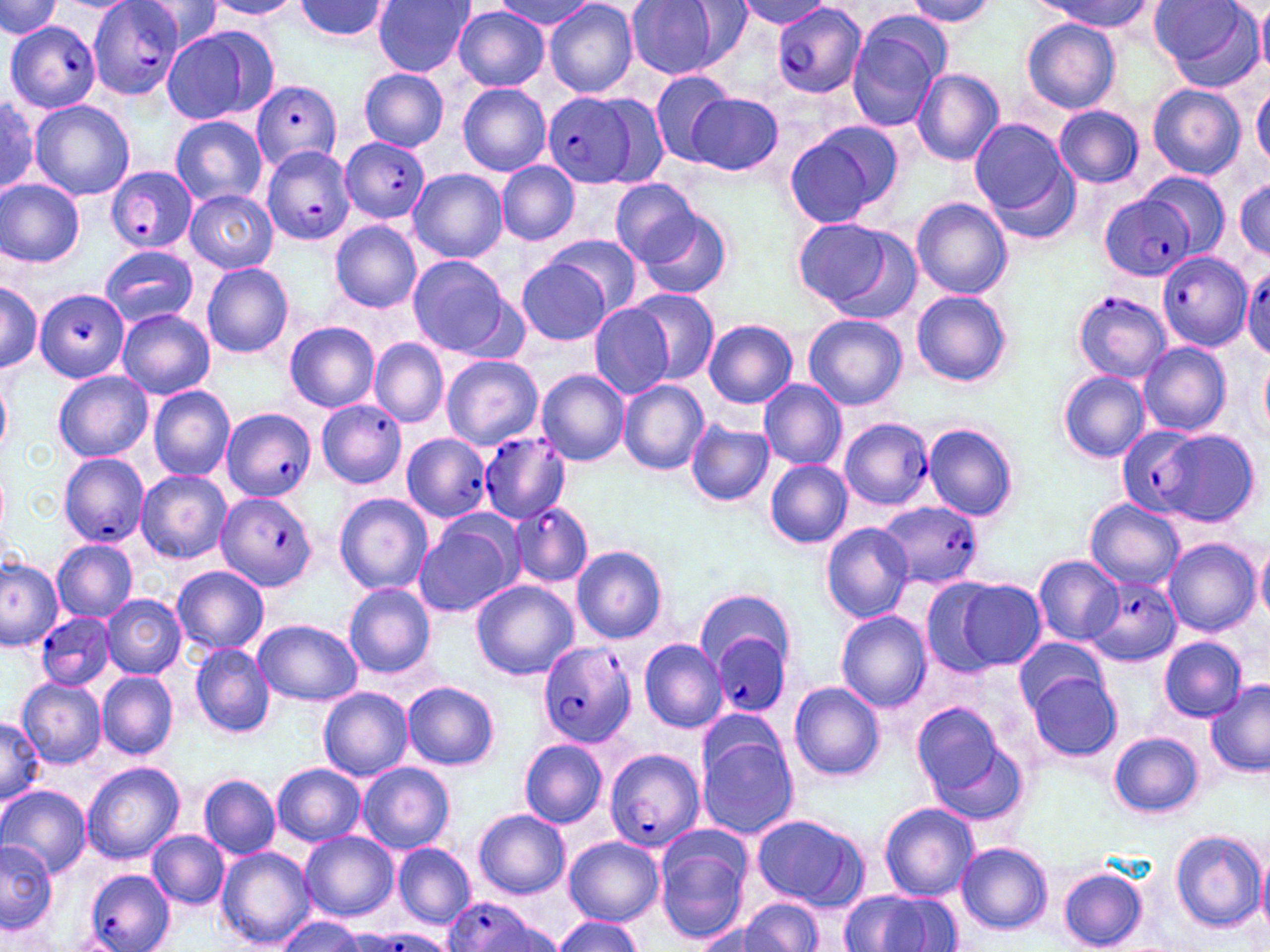

{
  "slide_level_diagnosis": "Plasmodium falciparum",
  "image_size": "1270×952 pixels",
  "uninfected_red_blood_cell_locations": "approximate bounding boxes as (x1,y1)-(x2,y2) corner pairs in pixels: (0,0)-(59,38), (287,0)-(396,44), (497,0)-(596,31), (627,0)-(724,79), (732,0)-(833,30), (1039,0)-(1151,32), (1153,0)-(1265,91), (134,1)-(227,53), (201,1)-(302,20), (371,1)-(475,76), (544,1)-(638,98), (907,1)-(994,28), (681,2)-(753,69), (1255,3)-(1270,76), (452,6)-(549,90), (847,16)-(948,131), (1022,18)-(1120,113), (159,25)-(277,127), (864,41)-(981,156), (913,68)-(1004,167), (360,69)-(449,149), (647,69)-(737,167), (458,82)-(551,175), (1148,83)-(1245,179), (1251,83)-(1270,170), (686,92)-(783,176), (0,97)-(45,197), (29,100)-(134,203), (1055,105)-(1143,188), (171,115)-(268,207), (969,119)-(1078,228), (784,122)-(900,228), (498,161)-(579,245), (408,168)-(507,263), (1140,170)-(1229,260), (1234,177)-(1269,259), (0,179)-(85,267), (610,180)-(702,266), (185,190)-(278,273), (913,197)-(1011,298), (633,206)-(734,301), (789,215)-(917,320), (330,220)-(421,312), (544,234)-(642,319), (100,246)-(198,327), (406,254)-(517,358), (515,259)-(613,346), (201,263)-(293,358), (0,282)-(42,371), (626,287)-(720,385), (912,290)-(1012,386), (589,304)-(673,397), (117,310)-(214,399), (803,314)-(908,410), (703,319)-(798,407), (285,322)-(379,412), (370,339)-(447,427), (1137,342)-(1230,437), (1258,353)-(1270,439), (441,355)-(543,449), (536,369)-(629,466), (1057,370)-(1151,464), (54,371)-(152,462), (0,376)-(11,456), (618,379)-(709,475), (758,379)-(846,470), (149,385)-(235,481), (687,421)-(774,507), (922,423)-(1021,521), (1155,427)-(1260,526), (765,461)-(853,548), (136,470)-(231,563), (333,492)-(434,595), (1085,499)-(1184,590), (413,515)-(522,617), (821,522)-(913,624), (1164,538)-(1259,636), (51,539)-(137,622), (1255,542)-(1270,624), (572,545)-(669,644), (1032,555)-(1123,644), (0,558)-(63,651), (172,566)-(270,656), (942,579)-(1048,671), (342,581)-(436,677), (472,581)-(578,680), (694,589)-(793,673), (101,595)-(185,677), (837,612)-(931,711), (252,618)-(361,706), (1160,636)-(1247,720), (1014,637)-(1106,715), (639,639)-(728,733), (191,642)-(275,738), (97,673)-(177,759), (1027,673)-(1121,761), (15,677)-(106,769), (402,681)-(500,771), (1205,682)-(1270,779), (789,683)-(885,781), (318,687)-(412,781), (911,701)-(1026,823), (696,708)-(785,786), (0,718)-(46,807), (1109,731)-(1203,817), (698,737)-(798,839), (519,739)-(608,827), (82,762)-(184,865), (357,762)-(455,853), (273,763)-(365,845), (199,776)-(279,859), (0,785)-(91,879), (879,801)-(978,899), (473,810)-(570,898), (749,814)-(868,910), (654,824)-(755,944), (148,830)-(228,908), (302,831)-(398,923), (1170,831)-(1267,933), (563,836)-(665,925), (2,840)-(57,934), (392,843)-(477,928), (957,843)-(1053,935), (215,845)-(317,948), (1257,849)-(1270,939), (1058,867)-(1147,951), (841,888)-(963,951), (740,899)-(824,950), (698,913)-(793,952), (279,914)-(363,952), (551,915)-(644,952)",
  "preparation": "thin blood smear",
  "stain": "May-Grünwald-Giemsa",
  "plasmodium_falciparum_infected_red_blood_cell_locations": "approximate bounding boxes as (x1,y1)-(x2,y2) corner pairs in pixels: (769,2)-(867,102), (84,4)-(185,102), (7,20)-(102,115), (251,80)-(341,172), (542,90)-(648,190), (340,137)-(433,224), (261,146)-(355,247), (105,165)-(196,254), (1102,193)-(1194,280), (1157,253)-(1253,350), (1242,266)-(1270,361), (1073,288)-(1170,383), (35,289)-(127,383), (316,400)-(407,488), (221,407)-(317,498), (839,417)-(933,511), (1115,424)-(1214,522), (477,432)-(572,523), (402,433)-(492,523), (59,452)-(149,548), (217,492)-(317,592), (510,501)-(592,588), (878,502)-(985,587), (1085,574)-(1182,666), (36,611)-(115,691), (710,633)-(788,716), (536,640)-(637,750), (606,748)-(704,853), (84,869)-(175,952), (442,898)-(547,952), (356,929)-(457,952)",
  "modality": "light microscopy",
  "field_of_view": "one of a larger specimen",
  "magnification": "1000x"
}